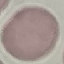
Result: negative for malaria parasites. Thin blood film. Acquired by smartphone through the microscope eyepiece. Giemsa-stained preparation. Cell patch, automatically extracted from a larger field of view and resized to 64 × 64 pixels.